Give the position of every malaria parasite and every leukocyte.
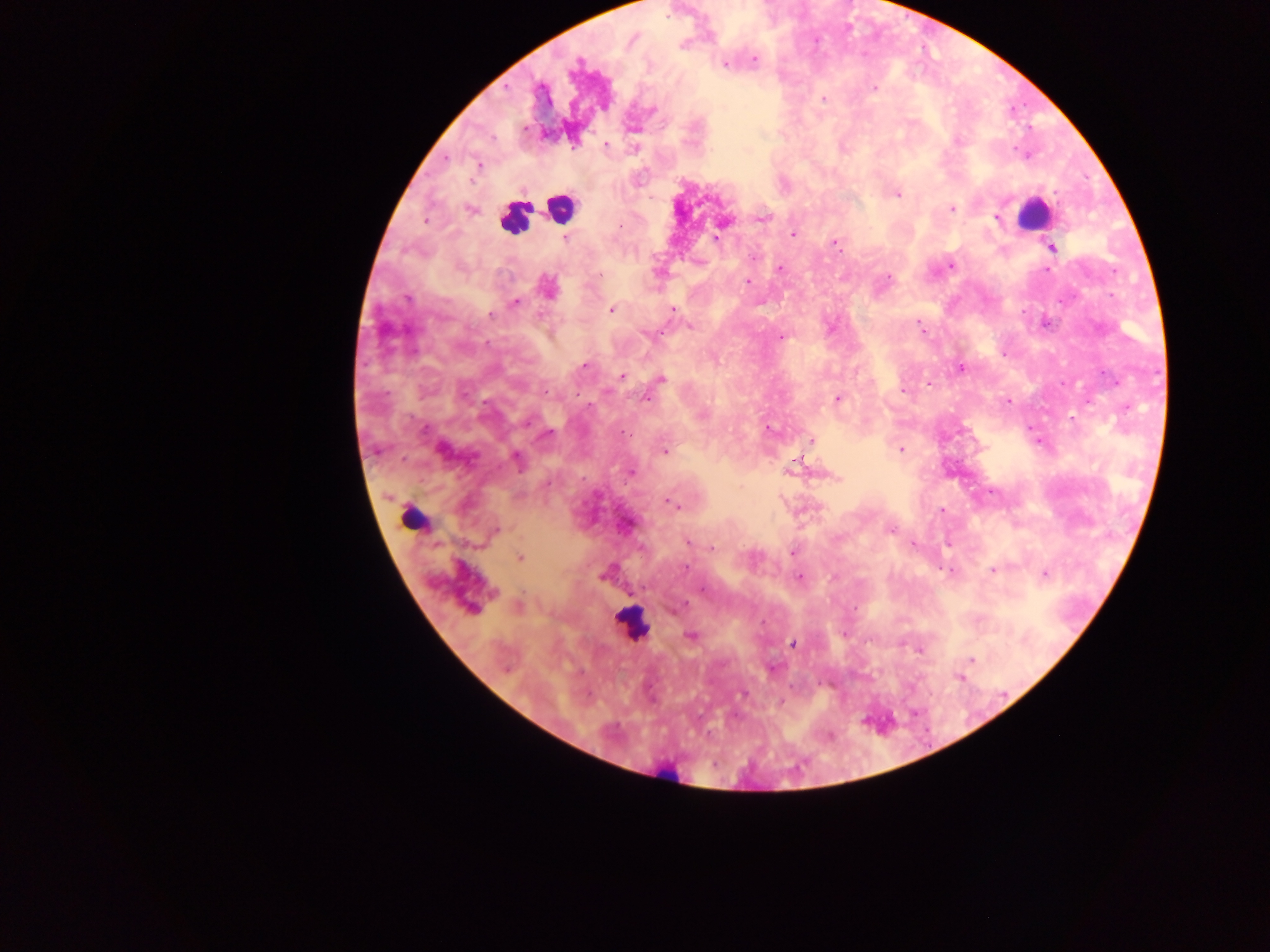

Approximate centers as [x, y] in pixels.
Malaria parasites: [755, 59], [577, 63], [725, 65], [874, 88], [824, 99], [652, 110], [526, 129], [958, 141], [606, 144], [478, 166], [898, 194], [952, 208], [469, 209], [762, 218], [996, 219], [425, 221], [793, 235], [565, 238], [716, 239], [836, 244], [1052, 248], [753, 256], [950, 265], [780, 268], [1046, 270], [600, 276], [888, 278], [748, 282], [548, 286], [407, 299], [515, 302], [611, 309], [672, 309], [491, 315], [691, 326], [920, 327], [651, 334], [781, 338], [584, 365], [961, 368], [622, 376], [662, 379], [929, 382], [904, 391], [647, 398], [838, 398], [1008, 401], [767, 428], [423, 429], [546, 435], [812, 441], [900, 450], [666, 451], [517, 459], [798, 461], [631, 472], [669, 503], [942, 510], [496, 531], [890, 531], [687, 541], [713, 547], [793, 553], [520, 557], [685, 568], [992, 570], [1045, 574], [603, 576], [799, 578], [703, 590], [677, 608], [690, 636], [793, 643], [972, 659], [773, 668], [743, 694].
Leukocytes: [561, 208], [1032, 214], [515, 218], [413, 519], [632, 624], [667, 775].

Summary:
  - Image size: 1270×952 pixels
  - Preparation: thick blood film
  - Field of view: single
  - Capture: mobile-phone photograph through a microscope
  - Country: Ghana